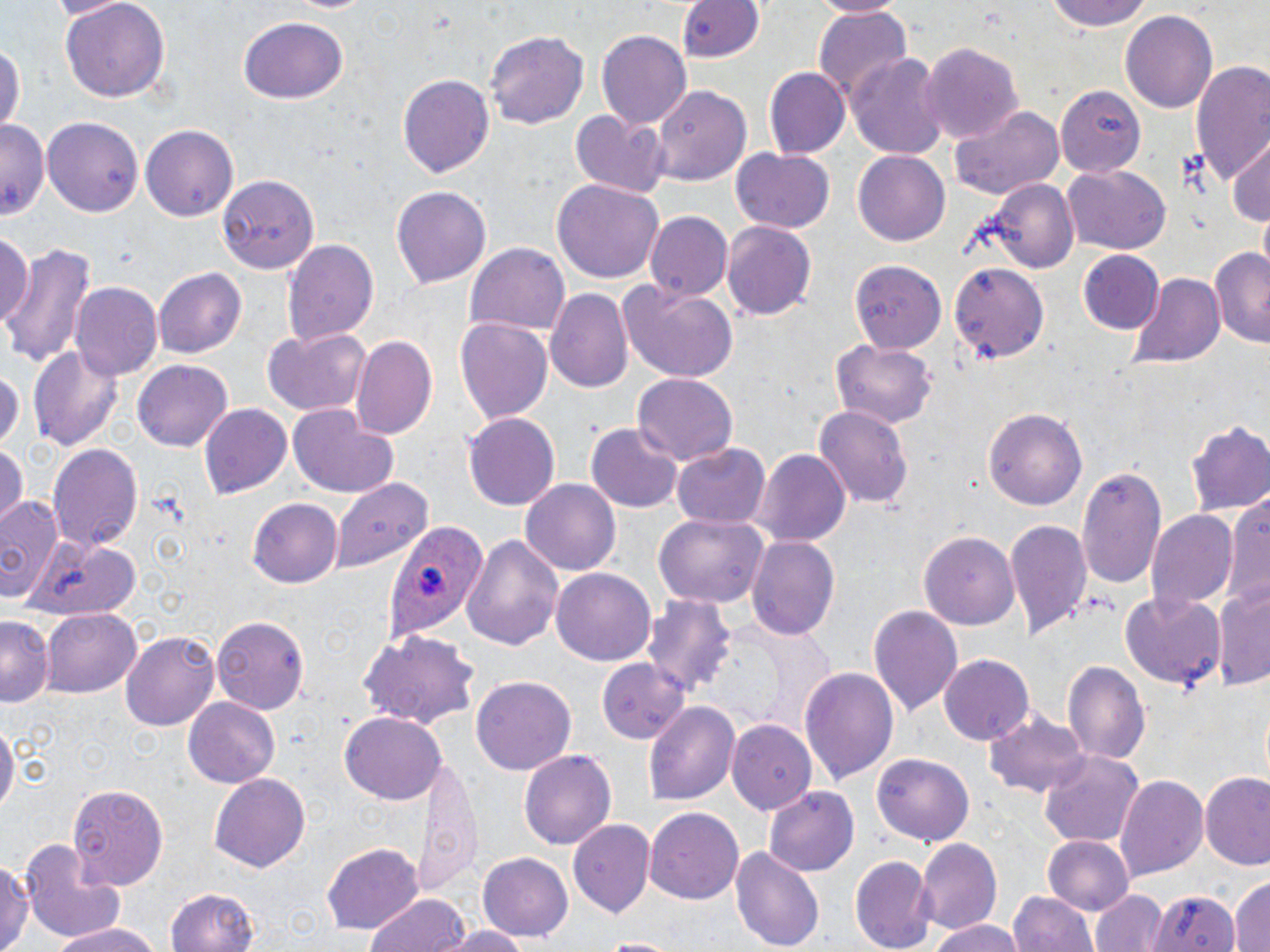 Approximate bounding boxes as (x1,y1)-(x2,y2) corner pairs in pixels. Uninfected red blood cell locations: (48,0)-(130,19), (59,0)-(170,104), (675,0)-(766,67), (813,0)-(908,17), (1048,0)-(1154,33), (280,1)-(375,16), (812,7)-(913,104), (1121,10)-(1218,114), (239,17)-(348,105), (596,28)-(691,127), (484,29)-(590,130), (0,36)-(23,139), (920,41)-(1024,145), (849,50)-(948,161), (1190,62)-(1270,190), (763,68)-(847,157), (397,73)-(495,180), (651,82)-(753,186), (1053,85)-(1147,180), (948,105)-(1066,200), (570,110)-(669,195), (44,115)-(146,218), (0,120)-(48,218), (140,123)-(240,221), (1226,139)-(1270,230), (731,148)-(836,233), (853,149)-(951,248), (1062,164)-(1171,255), (216,174)-(319,274), (552,179)-(663,288), (982,180)-(1078,275), (391,185)-(493,289), (645,210)-(733,300), (723,219)-(816,320), (0,229)-(36,334), (285,238)-(379,349), (0,241)-(96,368), (464,243)-(569,337), (1207,245)-(1270,348), (1077,250)-(1164,335), (847,256)-(948,355), (949,261)-(1049,363), (153,268)-(245,359), (1128,272)-(1224,370), (618,281)-(739,381), (71,282)-(163,382), (547,287)-(634,394), (453,317)-(553,424), (261,328)-(373,416), (351,333)-(438,442), (830,338)-(937,429), (26,345)-(122,451), (133,360)-(233,452), (0,364)-(23,457), (633,374)-(737,465), (815,403)-(913,514), (200,404)-(292,501), (290,405)-(397,499), (984,409)-(1087,509), (463,412)-(561,511), (583,421)-(684,516), (1186,421)-(1270,517), (0,441)-(26,531), (47,441)-(143,552), (672,443)-(769,531), (754,449)-(849,550), (1074,462)-(1168,593), (520,478)-(622,576), (332,479)-(431,574), (1227,489)-(1270,613), (1,495)-(66,605), (248,499)-(341,589), (1146,509)-(1237,609), (654,513)-(767,608), (1004,517)-(1093,639), (920,530)-(1021,630), (461,533)-(564,651), (24,535)-(143,617), (746,536)-(840,640), (552,569)-(656,665), (1215,582)-(1270,692), (1120,590)-(1225,688), (644,596)-(736,701), (867,604)-(964,719), (43,609)-(141,698), (212,614)-(309,713), (0,617)-(52,708), (358,628)-(481,730), (123,631)-(218,732), (936,648)-(1035,744), (600,658)-(691,744), (1064,660)-(1149,766), (800,667)-(898,787), (472,676)-(576,774), (184,697)-(280,789), (644,700)-(739,807), (341,713)-(446,804), (985,713)-(1089,798), (728,718)-(815,813), (0,720)-(17,818), (518,748)-(617,850), (1038,750)-(1142,846), (871,751)-(976,848), (412,754)-(484,896), (209,772)-(310,873), (1115,774)-(1208,879), (1201,775)-(1270,870), (66,783)-(168,889), (765,787)-(859,875), (644,806)-(746,906), (567,819)-(656,919), (1043,835)-(1133,914), (916,839)-(1002,934), (323,842)-(423,934), (22,843)-(128,941), (731,845)-(824,950), (478,853)-(572,944), (851,853)-(934,950), (0,856)-(31,952), (1231,873)-(1269,952), (164,888)-(261,952), (1093,888)-(1163,952), (1145,888)-(1240,952), (1009,889)-(1099,952), (366,894)-(470,952), (44,920)-(160,952), (929,920)-(1025,952), (443,924)-(532,952), (590,937)-(682,952). Plasmodium ovale-infected red blood cell locations: (389,519)-(489,637). Slide-level diagnosis: Plasmodium ovale. Optical microscopy. May-Grünwald-Giemsa-stained preparation. Thin blood smear. Single field of view. Image is 1270×952 pixels. 1000x magnification.